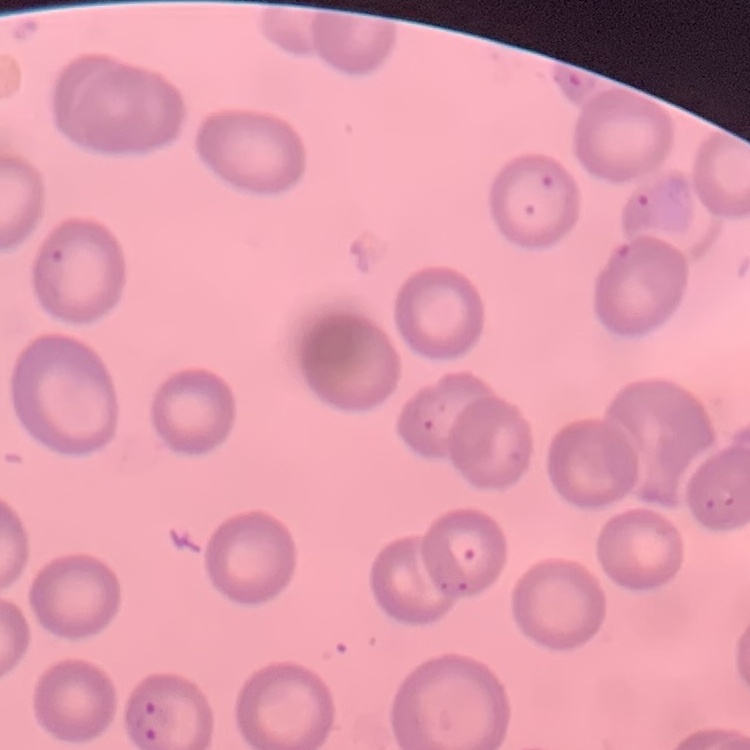
The red blood cells show no rouleaux formation. Square crop of a larger photomicrograph. Thin peripheral smear. Stained with either Field's or Giemsa.